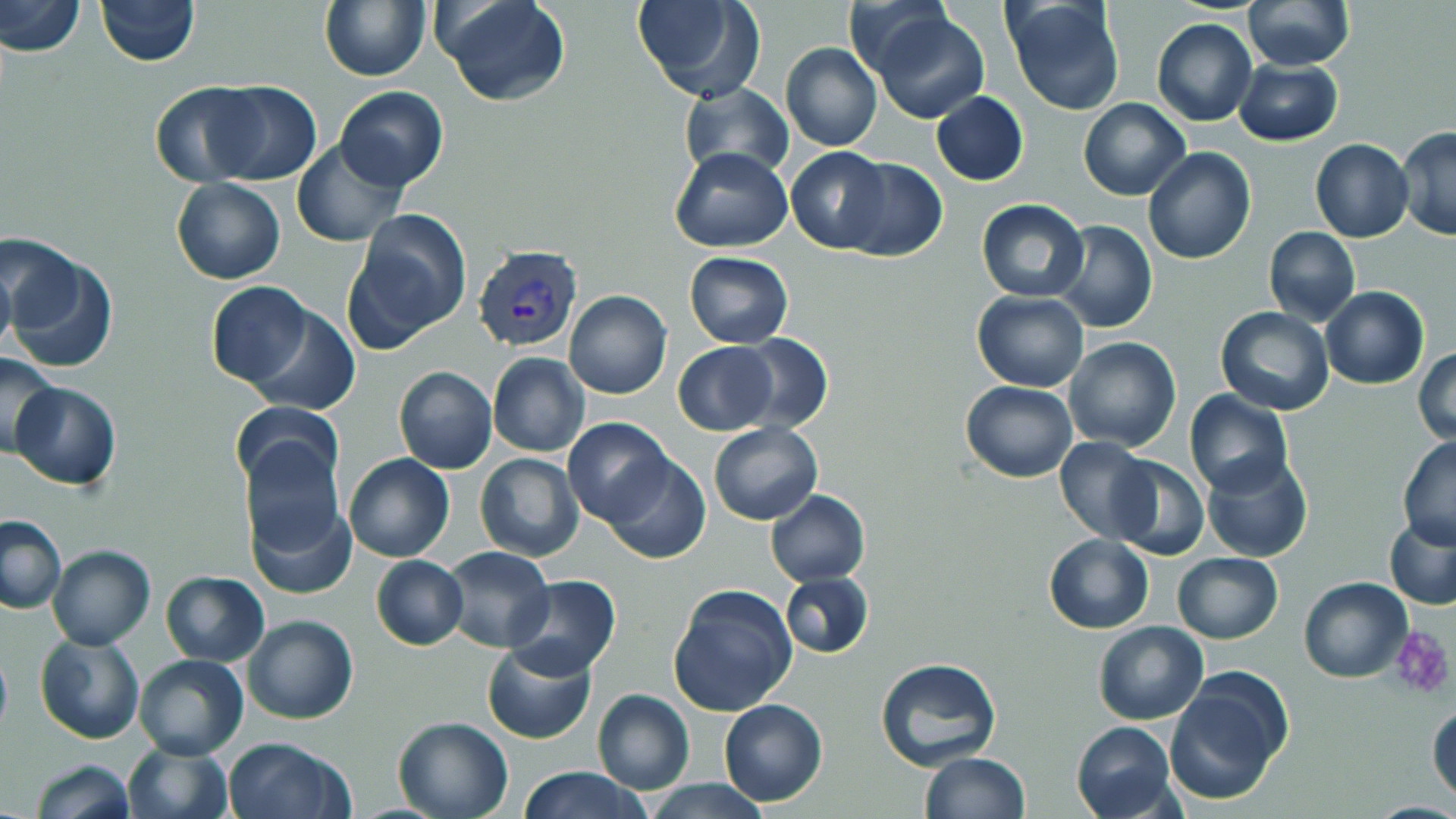

Approximate bounding boxes as named x1/y1/x2/y2 corners in pixels. Platelet locations: (x1=1389, y1=625, x2=1455, y2=698). Uninfected red blood cell locations: (x1=2, y1=0, x2=85, y2=56), (x1=95, y1=0, x2=199, y2=65), (x1=437, y1=0, x2=570, y2=106), (x1=632, y1=0, x2=766, y2=104), (x1=840, y1=0, x2=955, y2=83), (x1=1003, y1=0, x2=1127, y2=115), (x1=1242, y1=0, x2=1354, y2=71), (x1=320, y1=1, x2=429, y2=81), (x1=871, y1=9, x2=990, y2=124), (x1=1152, y1=18, x2=1257, y2=127), (x1=781, y1=42, x2=882, y2=152), (x1=1234, y1=58, x2=1343, y2=146), (x1=204, y1=80, x2=322, y2=186), (x1=150, y1=81, x2=263, y2=187), (x1=678, y1=81, x2=797, y2=181), (x1=335, y1=87, x2=449, y2=192), (x1=931, y1=91, x2=1028, y2=185), (x1=1078, y1=97, x2=1190, y2=201), (x1=1396, y1=127, x2=1456, y2=239), (x1=291, y1=139, x2=406, y2=247), (x1=1310, y1=139, x2=1414, y2=242), (x1=786, y1=145, x2=894, y2=253), (x1=670, y1=146, x2=794, y2=252), (x1=1142, y1=148, x2=1255, y2=264), (x1=837, y1=157, x2=949, y2=263), (x1=171, y1=179, x2=287, y2=285), (x1=976, y1=199, x2=1088, y2=302), (x1=346, y1=211, x2=471, y2=346), (x1=1051, y1=221, x2=1156, y2=333), (x1=1264, y1=227, x2=1361, y2=326), (x1=0, y1=243, x2=109, y2=373), (x1=683, y1=251, x2=793, y2=348), (x1=0, y1=253, x2=15, y2=360), (x1=206, y1=281, x2=314, y2=386), (x1=1320, y1=285, x2=1430, y2=389), (x1=564, y1=289, x2=672, y2=398), (x1=972, y1=292, x2=1089, y2=392), (x1=244, y1=303, x2=361, y2=415), (x1=1216, y1=307, x2=1333, y2=414), (x1=731, y1=333, x2=833, y2=434), (x1=1064, y1=337, x2=1181, y2=453), (x1=674, y1=342, x2=776, y2=435), (x1=1414, y1=347, x2=1456, y2=446), (x1=0, y1=353, x2=62, y2=458), (x1=487, y1=353, x2=591, y2=458), (x1=393, y1=366, x2=497, y2=474), (x1=960, y1=380, x2=1077, y2=482), (x1=11, y1=381, x2=121, y2=491), (x1=1185, y1=390, x2=1293, y2=496), (x1=231, y1=402, x2=342, y2=493), (x1=563, y1=417, x2=676, y2=527), (x1=709, y1=424, x2=822, y2=525), (x1=1053, y1=436, x2=1158, y2=543), (x1=1397, y1=437, x2=1456, y2=548), (x1=240, y1=438, x2=345, y2=562), (x1=1202, y1=450, x2=1313, y2=563), (x1=343, y1=453, x2=455, y2=561), (x1=475, y1=453, x2=585, y2=562), (x1=601, y1=454, x2=711, y2=564), (x1=1107, y1=456, x2=1209, y2=561), (x1=766, y1=490, x2=870, y2=585), (x1=245, y1=495, x2=358, y2=602), (x1=1, y1=515, x2=67, y2=614), (x1=1384, y1=517, x2=1456, y2=609), (x1=1044, y1=534, x2=1153, y2=633), (x1=47, y1=545, x2=156, y2=650), (x1=439, y1=546, x2=553, y2=651), (x1=1172, y1=551, x2=1284, y2=643), (x1=370, y1=555, x2=468, y2=650), (x1=159, y1=571, x2=269, y2=666), (x1=779, y1=571, x2=873, y2=659), (x1=505, y1=575, x2=621, y2=679), (x1=1300, y1=577, x2=1413, y2=683), (x1=667, y1=585, x2=797, y2=718), (x1=243, y1=615, x2=359, y2=725), (x1=1093, y1=621, x2=1209, y2=725), (x1=34, y1=633, x2=145, y2=744), (x1=0, y1=639, x2=12, y2=743), (x1=481, y1=639, x2=598, y2=744), (x1=134, y1=654, x2=249, y2=759), (x1=875, y1=656, x2=1001, y2=771), (x1=1166, y1=672, x2=1290, y2=805), (x1=592, y1=689, x2=694, y2=794), (x1=718, y1=698, x2=827, y2=806), (x1=1427, y1=698, x2=1455, y2=803), (x1=392, y1=716, x2=512, y2=819), (x1=1071, y1=721, x2=1177, y2=819), (x1=222, y1=736, x2=352, y2=819), (x1=123, y1=742, x2=232, y2=819), (x1=921, y1=751, x2=1031, y2=819), (x1=31, y1=759, x2=135, y2=819), (x1=515, y1=767, x2=650, y2=819), (x1=643, y1=778, x2=772, y2=818). Plasmodium vivax-infected red blood cell locations: (x1=472, y1=244, x2=584, y2=352). Slide-level diagnosis: Plasmodium vivax. Light microscopy. One field of a larger specimen. May-Grünwald-Giemsa stain. 1000x magnification. Thin blood film. Image is 1456×819 pixels.